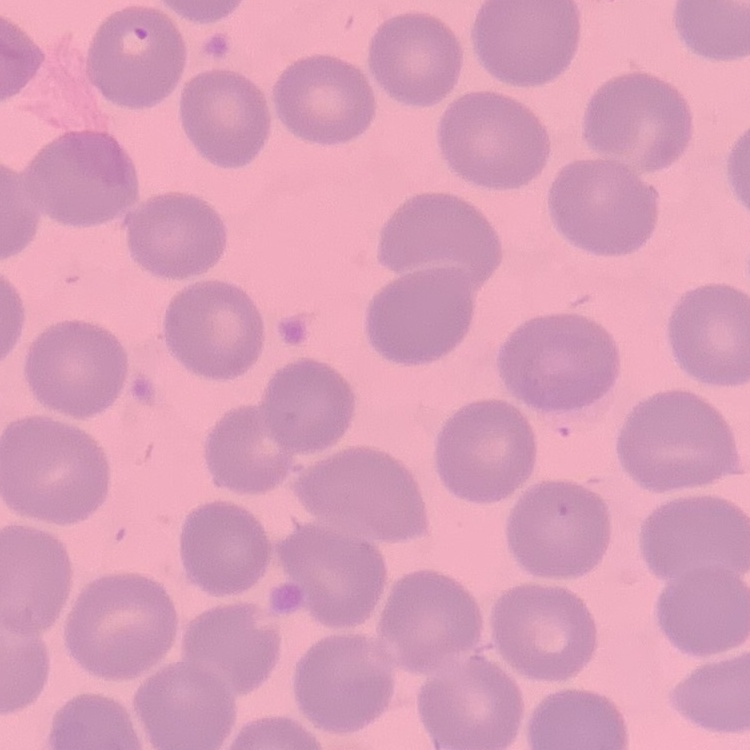

Summary:
  - Red blood cell morphology: no rouleaux formation
  - Stain: Field's or Giemsa
  - Preparation: thin peripheral smear
  - Image type: one tile cut from a larger photomicrograph